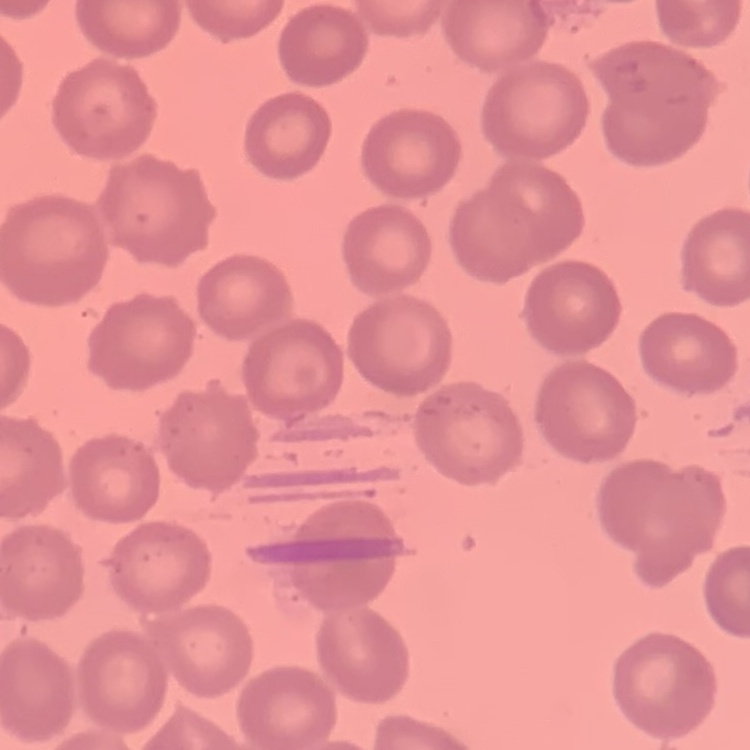
The red blood cells exhibit no rouleaux formation. Stained with either Field's or Giemsa. Thin blood film. One tile cut from a larger photomicrograph.